Assess this cell for malaria.
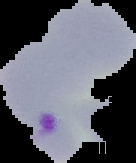

It is parasitized.

Cell region segmented out of the field of view; the surrounding area is masked to black. From a thin blood smear. Image is 136×163 pixels.